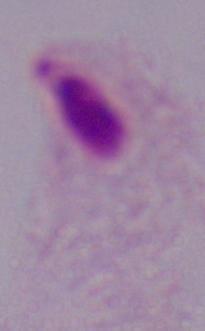
{
  "modality": "micrograph",
  "identification": "trichomonad",
  "magnification": "1000x"
}